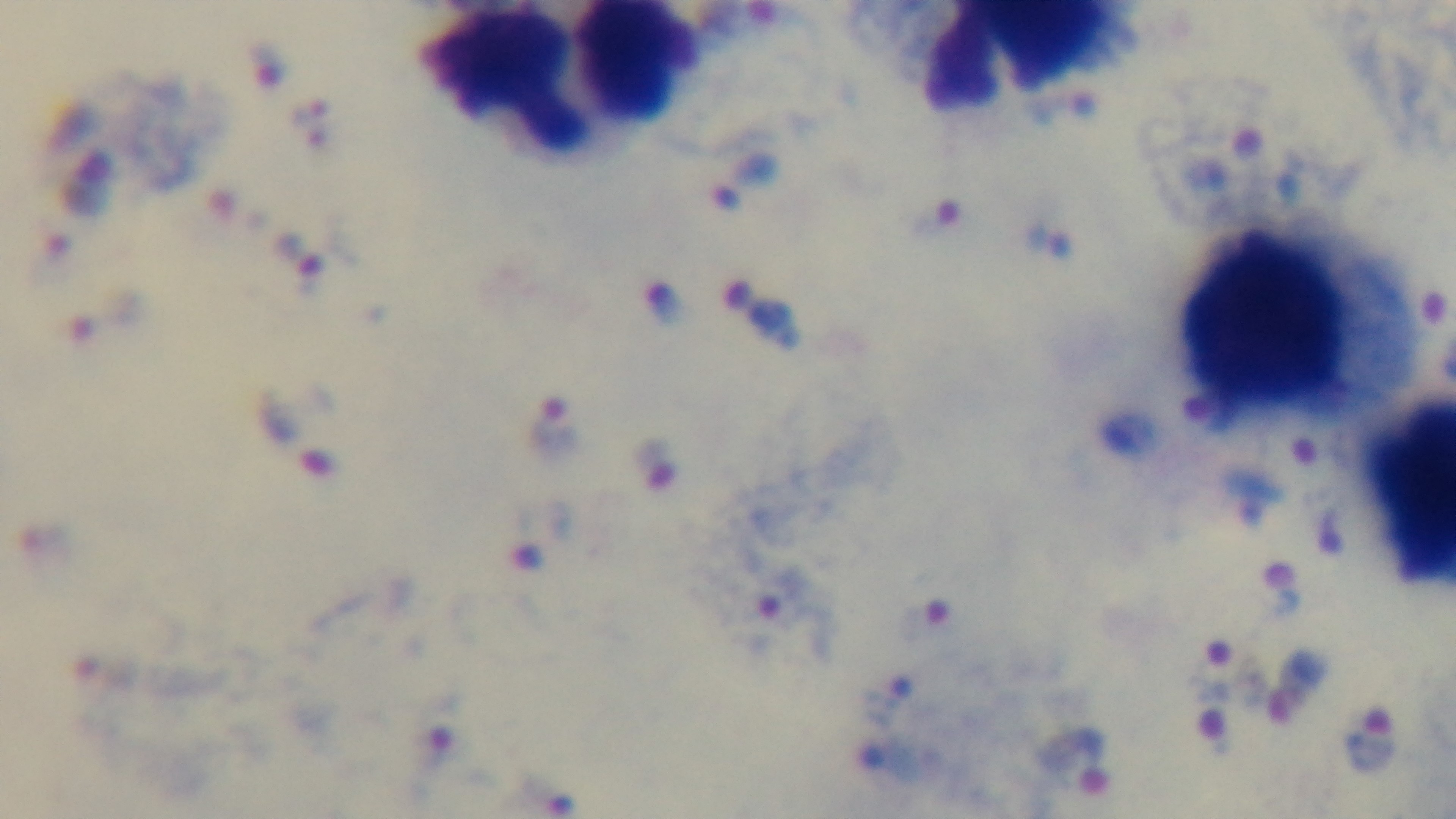

Summary:
  - Capture: mounted 4K digital camera
  - Field of view: single
  - Stain: Giemsa
  - Preparation: thick
  - Malaria status: positive
  - Objective: 100x oil immersion
  - Modality: light microscopy